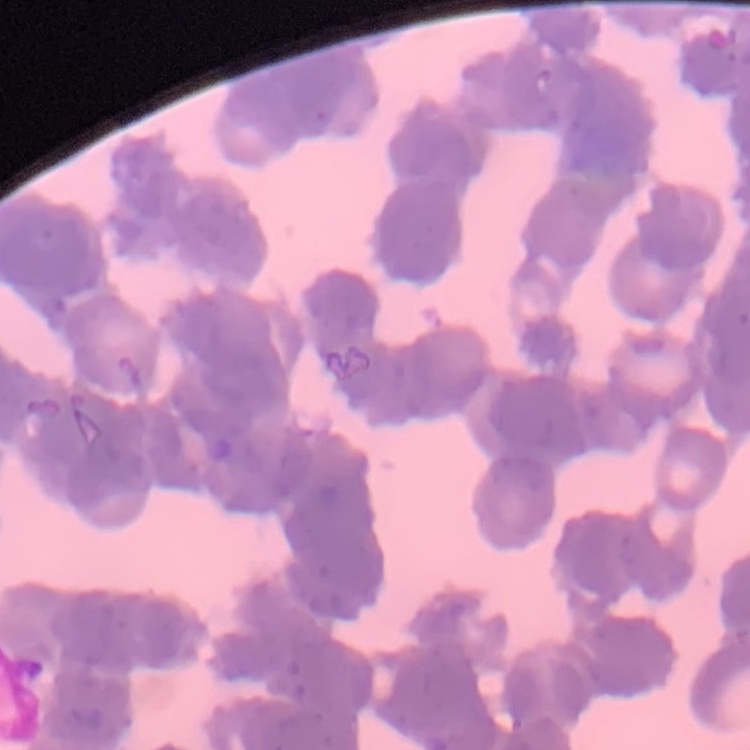

Summary:
  - Red blood cell morphology: rouleaux formation
  - Image type: one tile cut from a larger photomicrograph
  - Preparation: thin blood film
  - Stain: Field's or Giemsa